Classify this cell by malaria status.
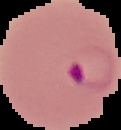
Parasitized.

Summary:
  - Image size: 121×130 pixels
  - Image type: cell region segmented out of the field of view; surrounding area masked to black
  - Preparation: thin blood film